Point out every malaria parasite.
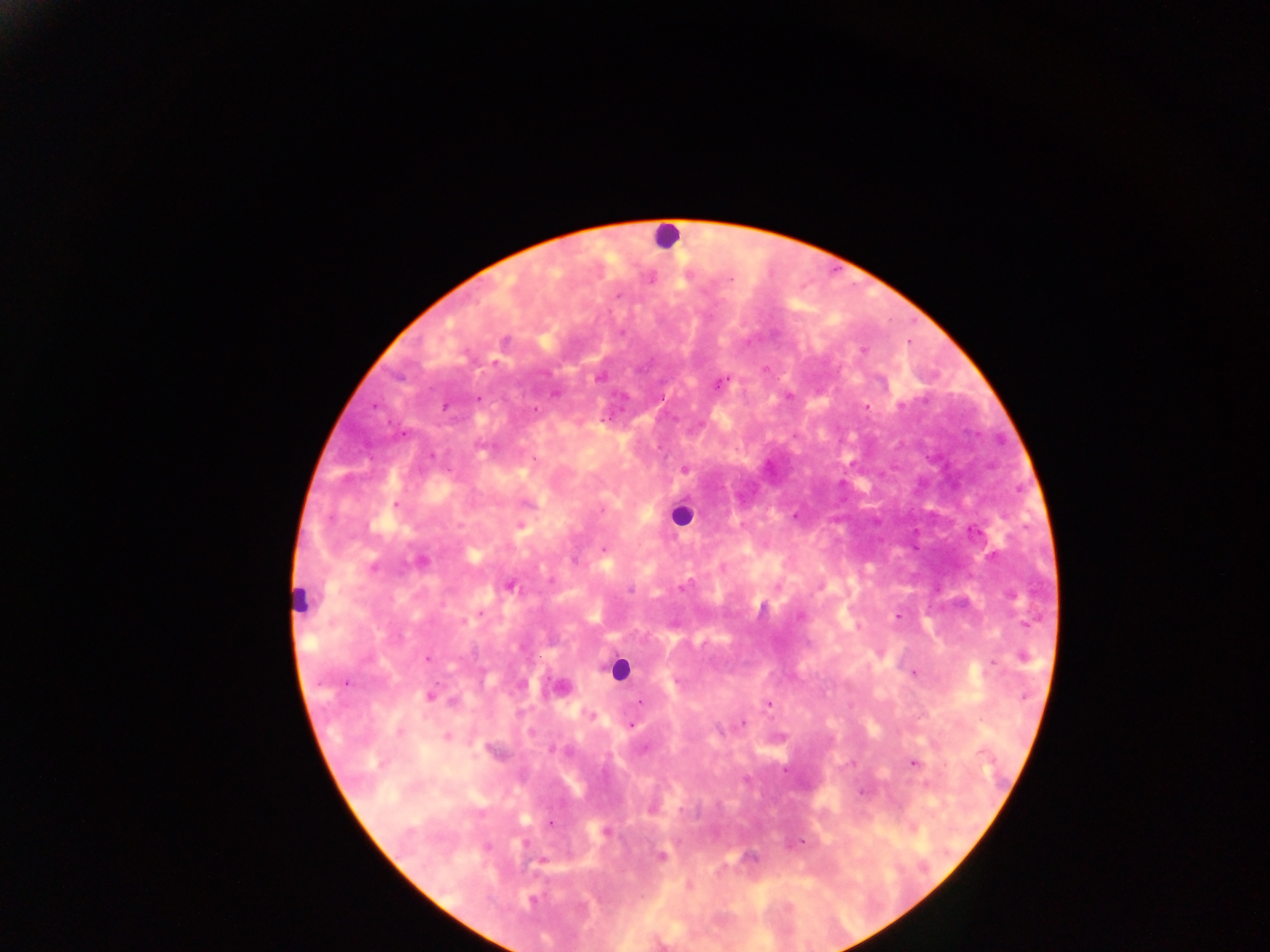

Approximate centers as x y in pixels.
Malaria parasites: 730 279; 618 295; 621 333; 505 341; 863 350; 765 370; 599 378; 719 383; 554 393; 789 397; 478 398; 445 406; 866 406; 901 406; 535 410; 483 447; 534 458; 685 469; 396 504; 527 504; 602 510; 460 525; 521 525; 974 532; 604 549; 421 561; 373 567; 550 581; 510 586; 683 587; 630 590; 1012 595; 480 613; 898 616; 799 617; 464 621; 1023 656; 428 659; 993 662; 913 673; 346 682; 431 696; 452 701; 639 702; 768 704; 591 715; 743 722; 631 725; 718 730; 400 732; 446 737; 495 751; 914 763; 785 770; 862 792; 551 824; 605 832; 802 842; 487 847; 661 856; 749 857; 541 861; 533 900.

preparation = thick blood smear
capture = mobile-phone photograph through a microscope
leukocyte locations = approximate centers as x y in pixels: 667 237; 681 515; 301 598; 617 669
image size = 1270×952 pixels
field of view = single
country = Ghana